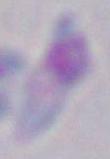

magnification = 1000x
modality = photomicrograph
identification = Toxoplasma gondii